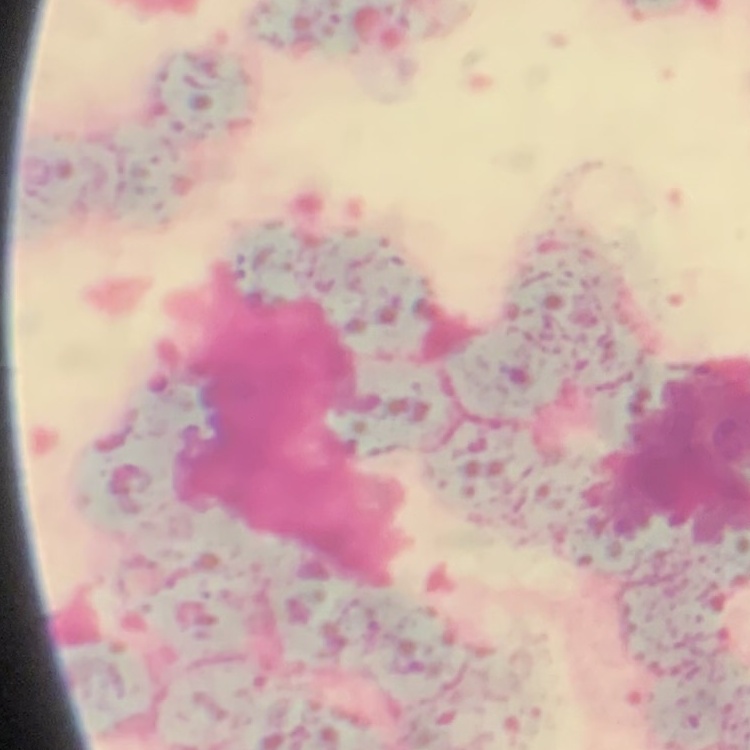
Summary:
  - Red blood cell morphology: rouleaux formation
  - Stain: Field's or Giemsa
  - Image type: one tile cut from a larger photomicrograph
  - Preparation: thin blood film